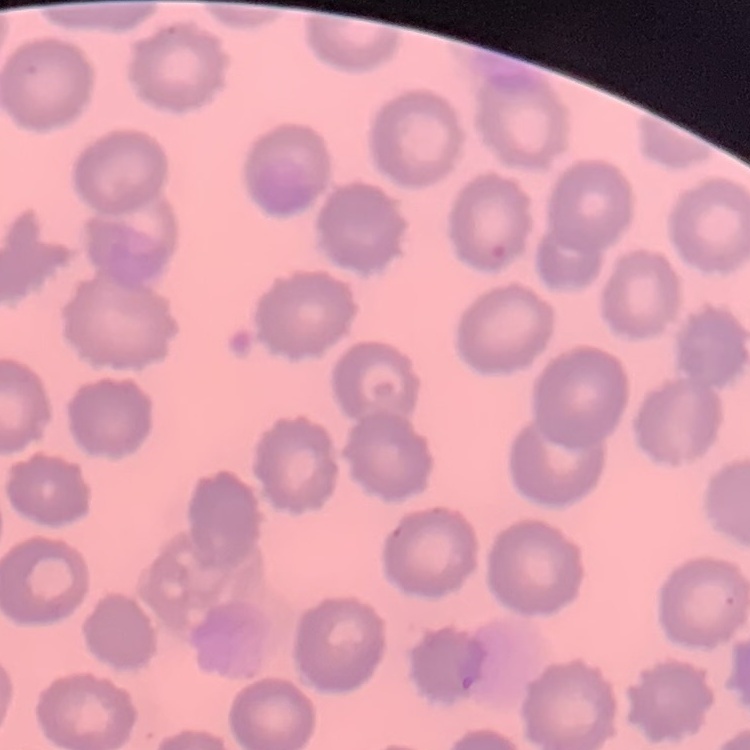

The red blood cells exhibit no rouleaux formation. Thin peripheral smear. Field's or Giemsa stain. Square crop of a larger photomicrograph.